Identify the parasite.
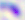

Toxoplasma gondii.

Captured at 400x magnification. Photomicrograph.